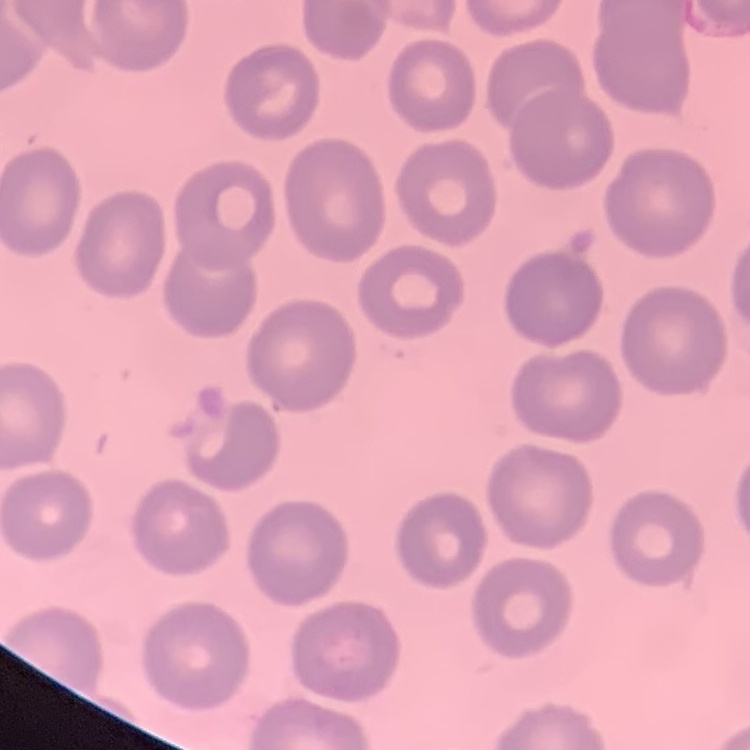 The erythrocytes exhibit no rouleaux formation. Thin blood film. Square crop of a larger photomicrograph. Field's or Giemsa stain.